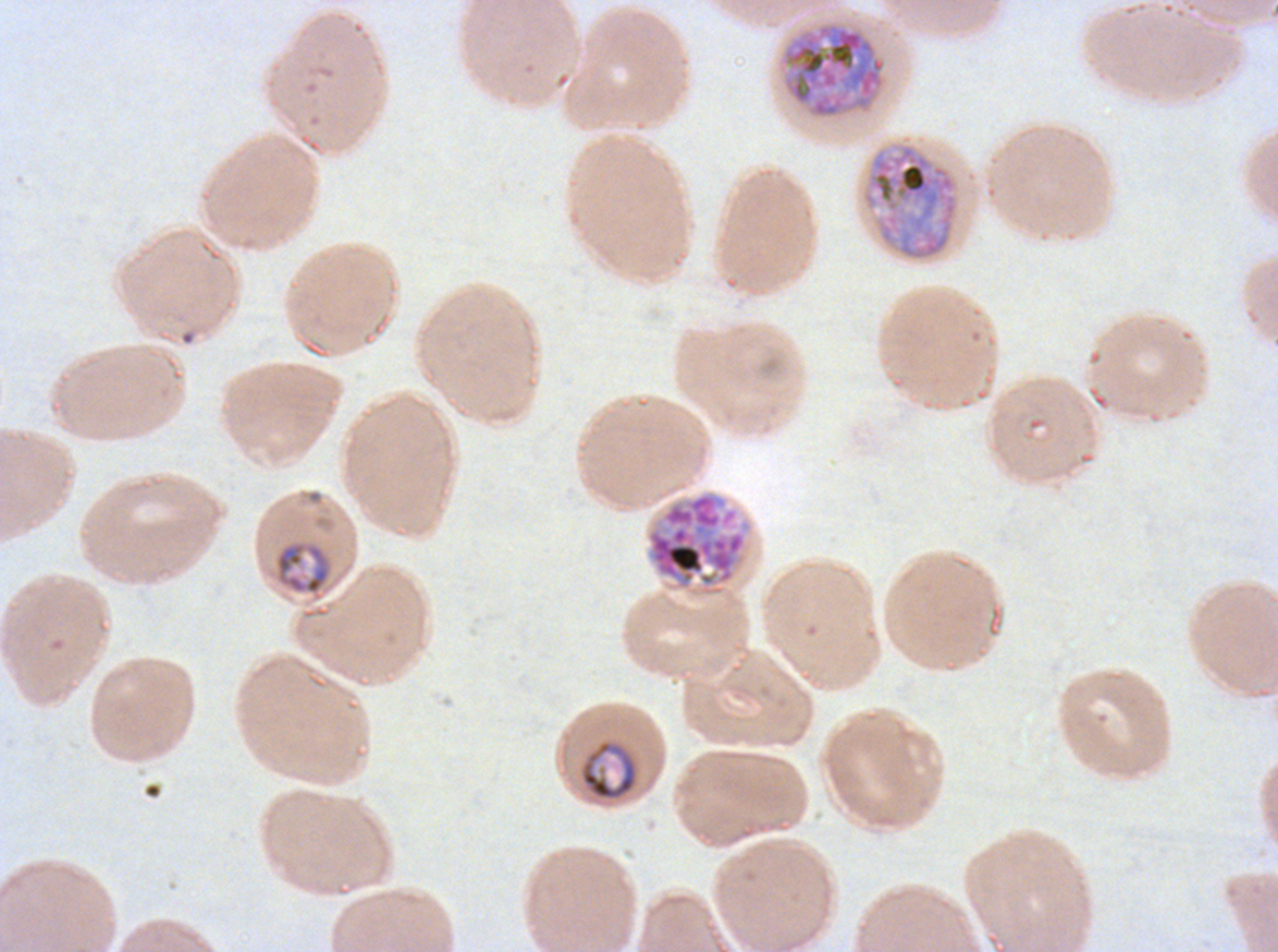
Approximate bounding boxes as (x1, y1, x2, y2) in pixels. Mid trophozoite locations: (274, 541, 332, 595), (580, 739, 638, 801). Late schizont locations: (780, 21, 887, 119), (862, 142, 958, 262), (645, 491, 747, 596). Plasmodium falciparum cultured ex vivo for 24 to 48 hours, from a patient in The Gambia. One sub-image of a larger composite. Thin blood smear. Giemsa-stained preparation. Image is 1278×952 pixels. Life-cycle stages observed: mid trophozoite, late schizont.